Draw a bounding box around every Plasmodium parasite, every leukocyte, and every artifact (stain precipitate or debris).
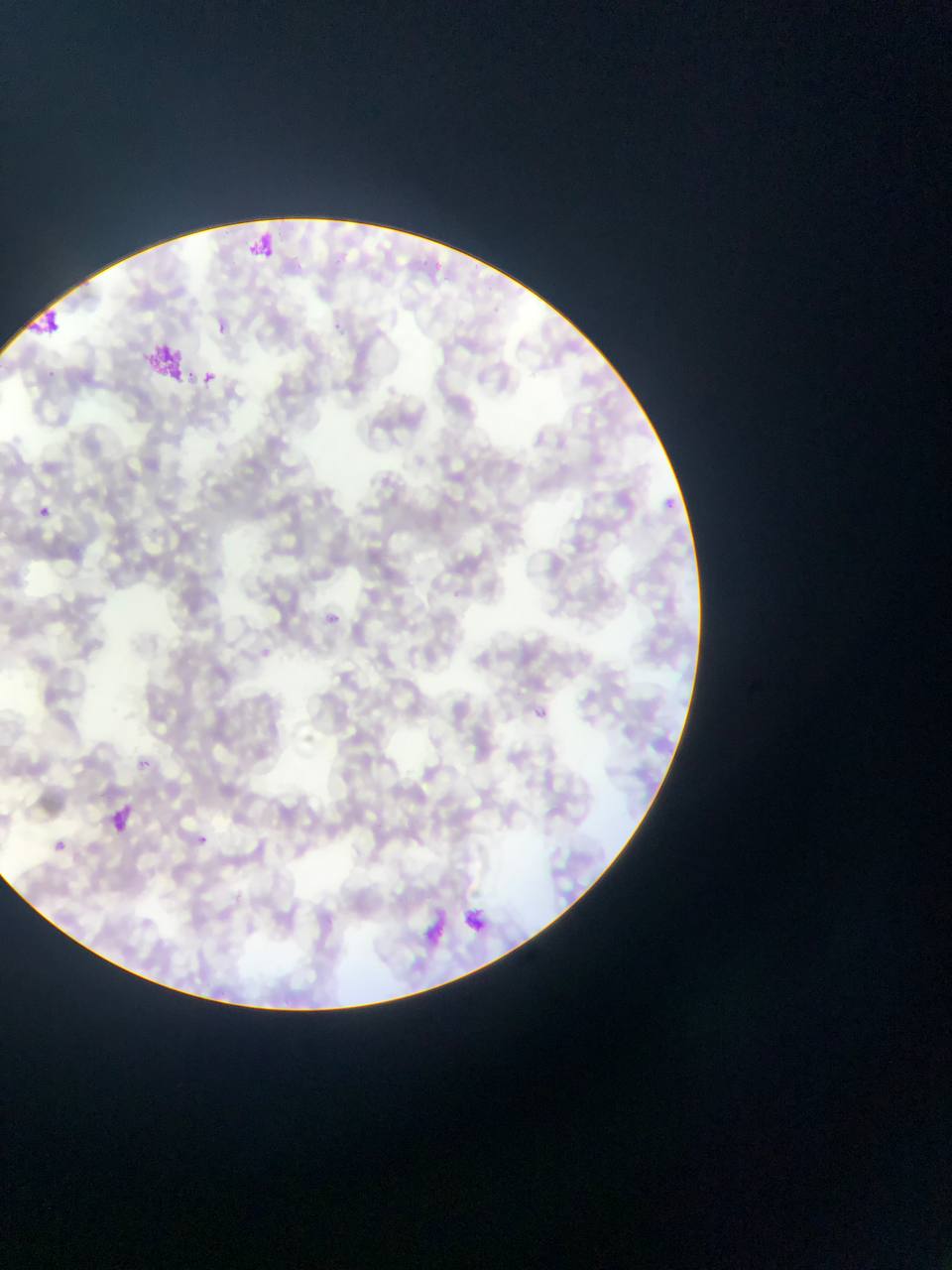

Approximate bounding boxes as left top right bottom in pixels.
Plasmodium parasites: 199 369 216 385; 656 483 691 518; 34 505 50 519; 322 609 365 642; 533 707 548 721; 132 755 152 774; 105 803 138 838; 188 829 213 851; 51 839 66 853.
Leukocytes: 241 227 280 266.
Artifacts (stain precipitate or debris): 26 309 66 339; 150 347 195 387; 421 900 449 953; 457 904 485 937.

country = Ghana
field of view = single
image size = 952×1270 pixels
preparation = thin blood film
capture = mobile-phone photograph through a microscope